Describe the morphology of the erythrocytes.
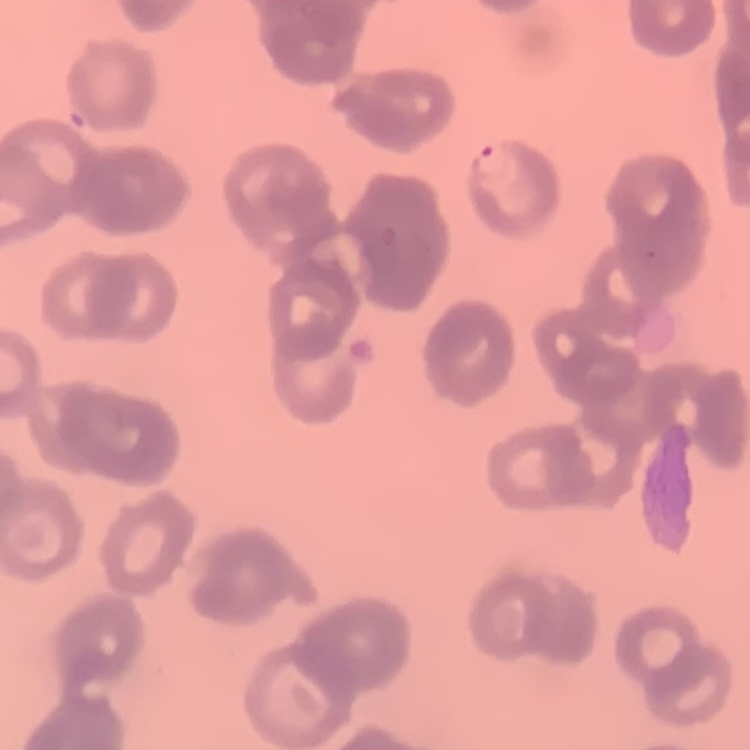
They show rouleaux formation.

Summary:
  - Image type: square crop of a larger photomicrograph
  - Preparation: thin blood smear
  - Stain: Field's or Giemsa